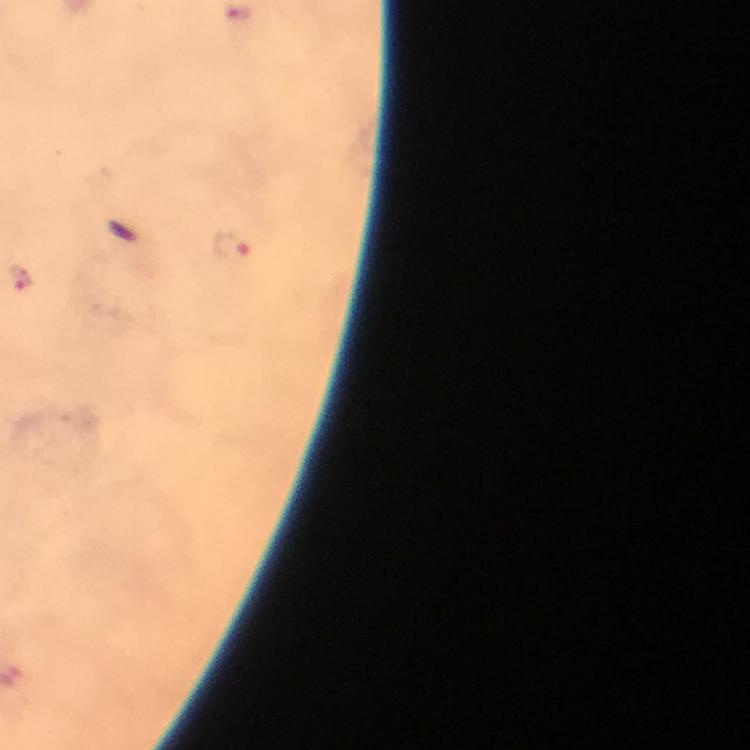
Approximate centers as [x, y] in pixels.
Summary:
  - Malaria parasite locations: [232, 246], [20, 279]
  - Context: from a malaria diagnostic workup
  - Immersion oil: applied
  - Cropped from: a single field of view
  - Stain: Giemsa
  - Image size: 750×750 pixels
  - Preparation: thick blood film
  - Capture: smartphone mounted on the microscope
  - Magnification: 100x